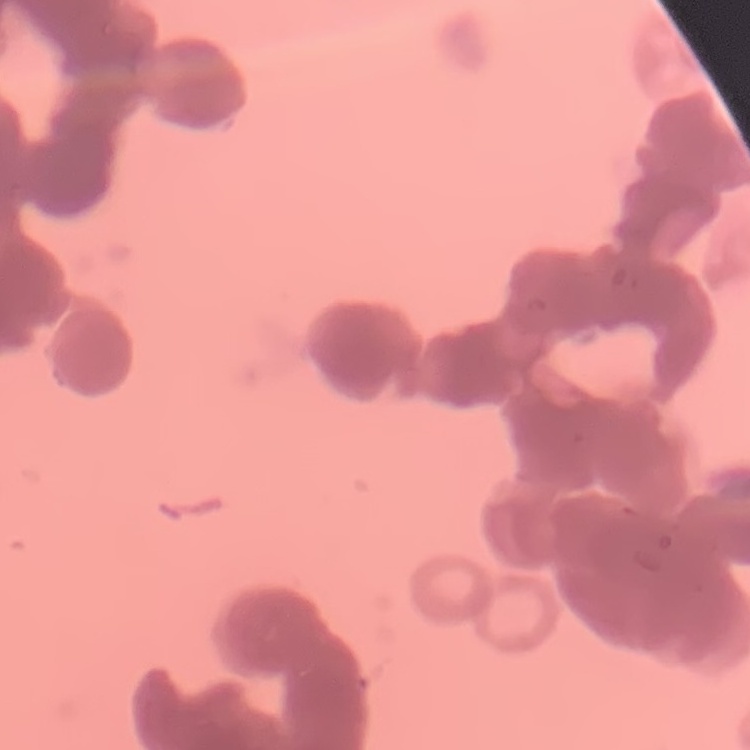
erythrocyte_morphology: rouleaux formation
stain: Field's or Giemsa
image_type: square crop of a larger photomicrograph
preparation: thin blood smear